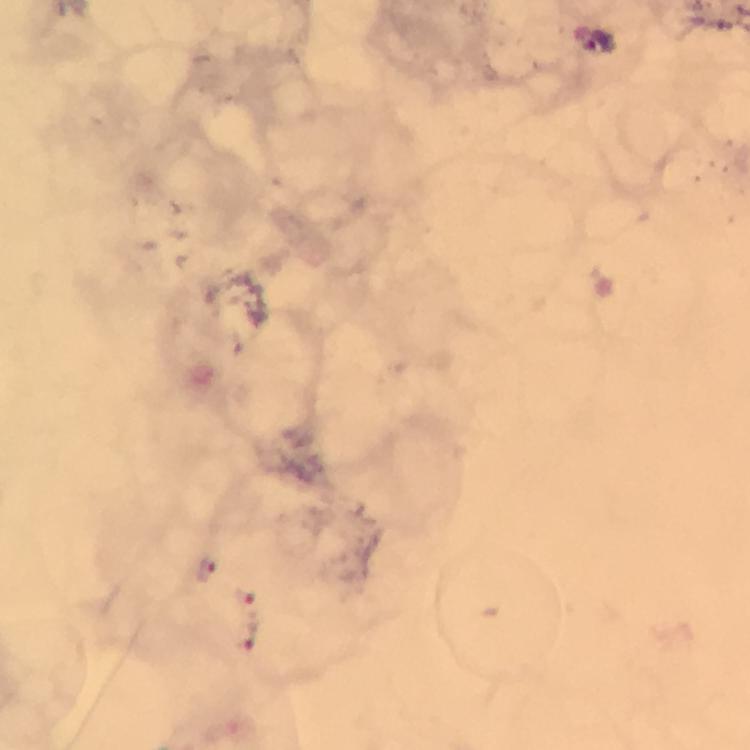
capture = smartphone mounted on the microscope
stain = Giemsa
cropped from = a single field of view
context = from a diagnostic examination for malaria
preparation = thick blood smear
magnification = 100x
image size = 750×750 pixels
immersion oil = used
Plasmodium parasite locations = approximate centers as [x, y] in pixels: [208, 572], [247, 595], [252, 638]